Identify the blood parasite species.
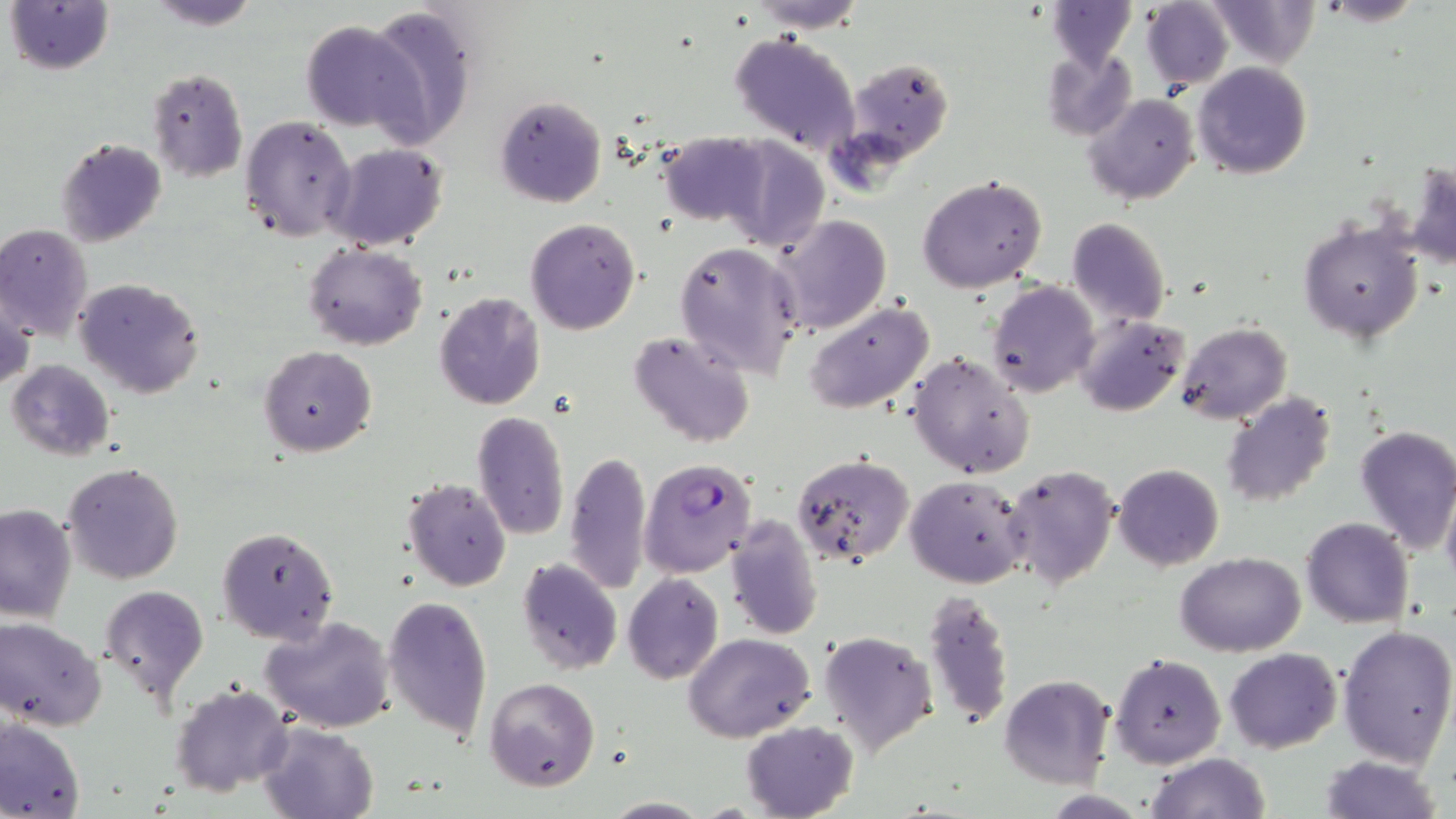
Plasmodium falciparum.

Approximate bounding boxes as (x1,y1)-(x2,y2) corner pairs in pixels. Uninfected red blood cell locations: (3,0)-(116,76), (146,0)-(261,30), (1142,0)-(1233,92), (1209,0)-(1319,69), (1316,0)-(1424,28), (1047,1)-(1136,67), (750,2)-(871,33), (363,5)-(477,148), (300,20)-(421,132), (728,30)-(861,155), (1041,49)-(1138,141), (840,55)-(957,172), (1194,61)-(1312,179), (145,67)-(248,182), (1085,93)-(1199,205), (495,95)-(607,207), (240,114)-(358,244), (659,132)-(768,226), (56,138)-(167,246), (726,140)-(828,251), (327,143)-(449,250), (1407,160)-(1456,272), (919,174)-(1047,292), (773,215)-(892,336), (1298,215)-(1423,345), (525,217)-(640,336), (1066,217)-(1172,327), (0,223)-(94,342), (673,241)-(804,379), (304,244)-(428,349), (73,278)-(206,399), (987,280)-(1099,398), (1,290)-(35,395), (432,291)-(547,411), (804,301)-(935,415), (1075,314)-(1189,417), (1175,322)-(1292,424), (628,330)-(756,449), (259,345)-(378,457), (907,352)-(1035,478), (6,359)-(115,460), (1220,392)-(1340,510), (472,411)-(570,540), (1354,424)-(1456,555), (564,450)-(652,595), (792,453)-(913,568), (61,462)-(184,584), (1114,463)-(1223,569), (1003,464)-(1120,591), (907,475)-(1032,588), (402,477)-(512,591), (1441,484)-(1456,592), (0,503)-(77,623), (726,515)-(824,640), (1301,516)-(1413,629), (216,525)-(340,645), (1176,552)-(1305,657), (516,557)-(623,674), (622,573)-(724,684), (100,585)-(209,704), (923,587)-(1014,731), (381,595)-(493,742), (1,615)-(109,730), (261,616)-(396,733), (1336,624)-(1455,767), (818,631)-(938,756), (686,632)-(815,742), (1224,648)-(1342,753), (1111,652)-(1226,769), (1000,675)-(1114,789), (484,678)-(600,792), (169,683)-(294,796), (0,719)-(86,819), (740,720)-(858,819), (258,721)-(379,819), (1144,753)-(1272,819), (1318,754)-(1443,819), (600,797)-(709,817). Plasmodium falciparum-infected red blood cell locations: (639,458)-(757,577). Thin blood smear. Image is 1456×819 pixels. Light microscopy. One field of a larger specimen. May-Grünwald-Giemsa-stained preparation. Captured at 1000x magnification.